Locate every malaria parasite.
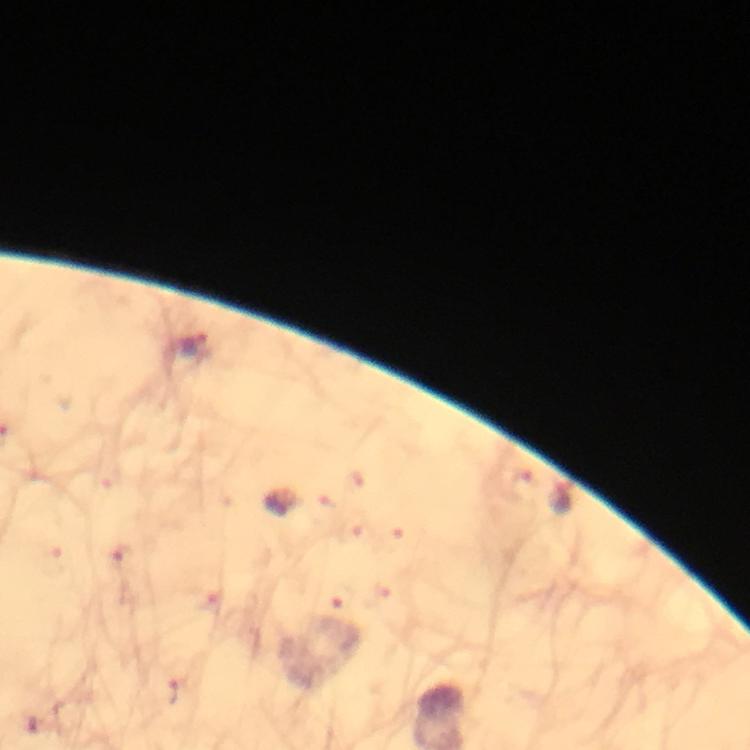

Approximate object centers, in pixels from the top-left corner.
Malaria parasites: (x=194, y=345).

Summary:
  - Preparation: thick smear
  - Cropped from: one field of view
  - Stain: Giemsa
  - Image size: 750×750 pixels
  - Magnification: 100x
  - Capture: smartphone camera through the microscope
  - Immersion oil: used
  - Context: from a diagnostic examination for malaria